Give the position of every Plasmodium falciparum parasite, noting its life-cycle stage.
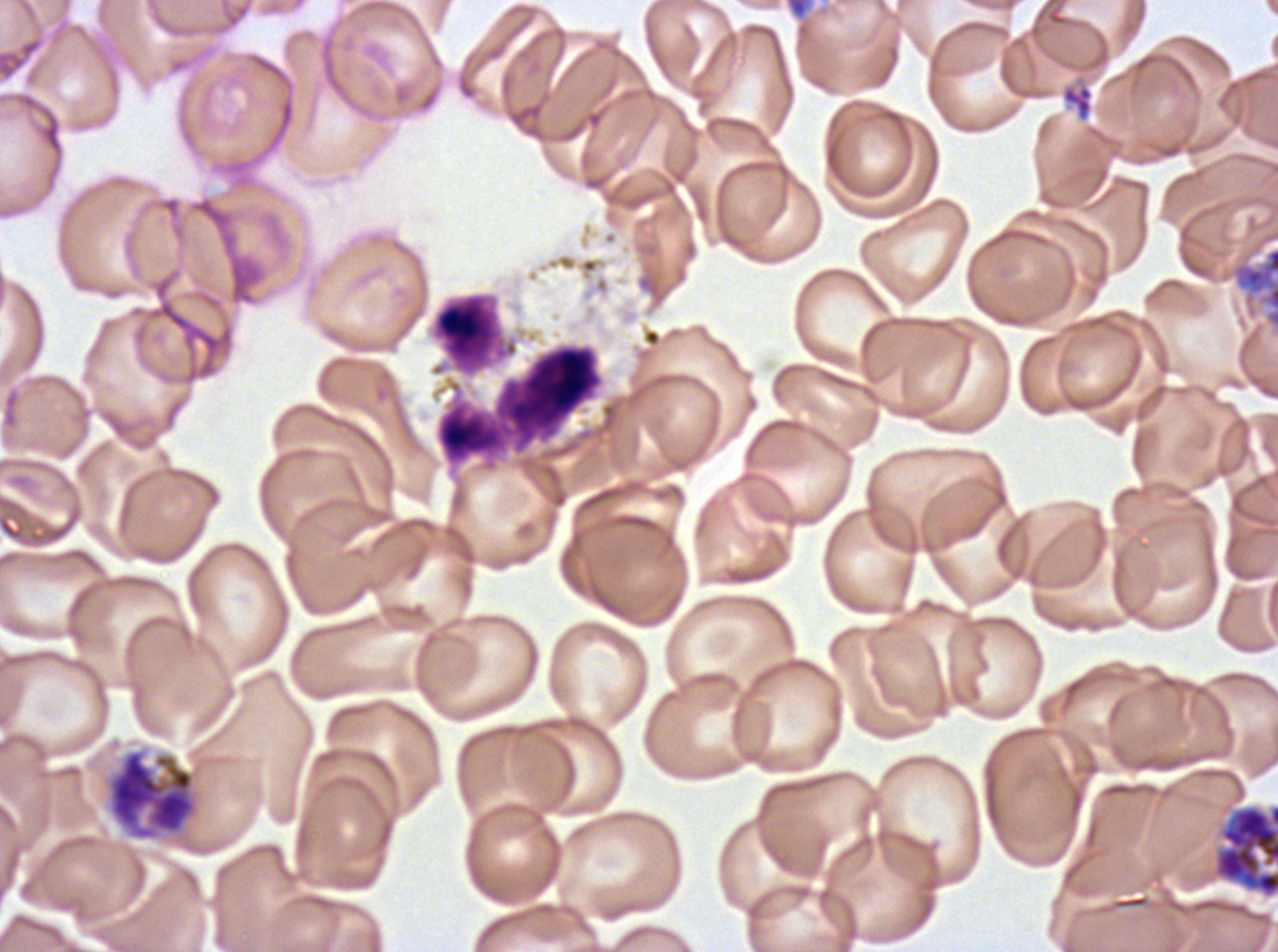

Approximate bounding boxes as {x1, y1, x2, y2} in pixels.
Early schizonts: {785, 0, 811, 19}, {105, 748, 200, 842}, {1211, 803, 1277, 899}.
Late schizonts: {1233, 247, 1277, 328}.
No rings, late-ring/early-trophozoite forms, mid trophozoites, late trophozoites, segmenters, or gametocytes observed.

Leukocyte locations: {433, 294, 502, 373}, {436, 344, 602, 464}. Debris locations: {1061, 83, 1094, 122}. A sub-image separated from a larger composite. Life-cycle stages observed: early schizont, late schizont. Thin blood film. Giemsa-stained preparation. Plasmodium falciparum cultured ex vivo for 24 to 48 hours, from a patient in The Gambia. Image is 1278×952 pixels.